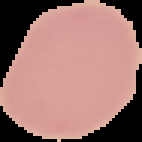
malaria status = uninfected
preparation = thin blood smear
image size = 142×142 pixels
image type = segmented cell region on a black background